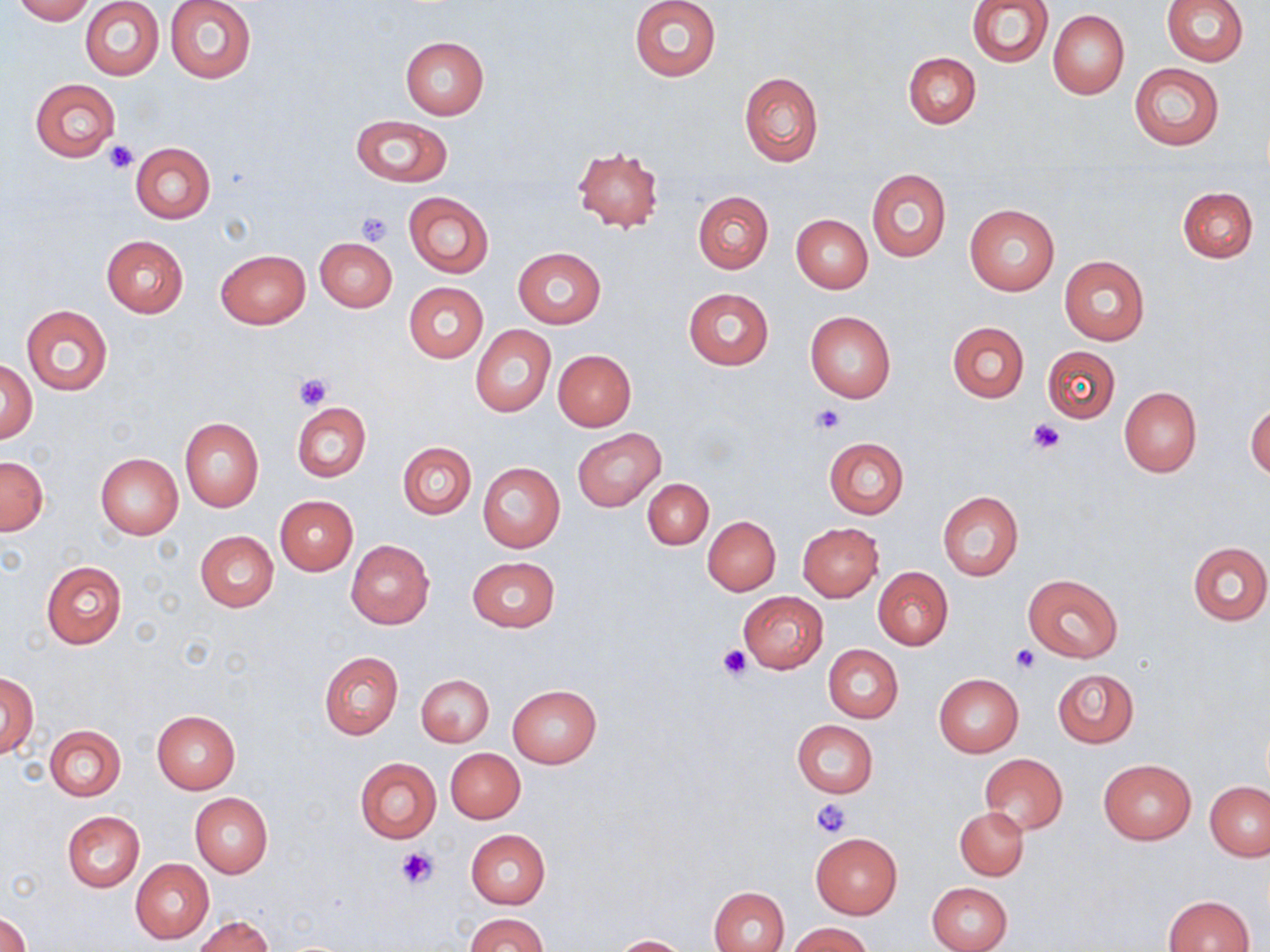
Summary:
  - Coordinate format: approximate bounding boxes as (x1, y1, x2, y2) in pixels
  - Platelet locations: (106, 139, 138, 173), (356, 210, 395, 245), (293, 373, 332, 410), (809, 405, 843, 433), (1027, 420, 1064, 454), (718, 645, 751, 680), (1012, 645, 1040, 672), (811, 798, 852, 839), (396, 845, 440, 889)
  - Uninfected red blood cell locations: (13, 0, 93, 23), (165, 0, 256, 83), (629, 0, 721, 82), (967, 0, 1053, 67), (1161, 0, 1248, 65), (81, 2, 164, 80), (1049, 9, 1129, 99), (401, 36, 489, 118), (904, 53, 980, 129), (1129, 63, 1224, 151), (739, 72, 823, 167), (31, 79, 119, 161), (350, 114, 454, 187), (129, 143, 215, 224), (572, 147, 664, 232), (866, 169, 951, 262), (1177, 187, 1258, 262), (404, 191, 493, 278), (693, 191, 773, 274), (964, 204, 1060, 295), (792, 214, 872, 293), (101, 236, 188, 317), (316, 237, 397, 312), (512, 248, 604, 329), (215, 249, 310, 328), (1059, 256, 1150, 345), (404, 283, 487, 362), (684, 287, 773, 370), (22, 305, 112, 395), (804, 311, 896, 402), (947, 320, 1029, 403), (470, 325, 555, 417), (1043, 345, 1119, 422), (553, 350, 636, 430), (1, 358, 36, 444), (1119, 387, 1201, 478), (1247, 401, 1270, 481), (292, 402, 371, 481), (179, 417, 264, 511), (572, 428, 666, 512), (825, 437, 909, 519), (398, 442, 476, 518), (96, 454, 183, 539), (1, 456, 48, 535), (477, 463, 565, 552), (642, 478, 714, 549), (937, 491, 1023, 580), (274, 495, 358, 575), (703, 515, 780, 596), (797, 522, 884, 601), (195, 531, 279, 611), (346, 540, 435, 629), (1187, 540, 1270, 625), (466, 556, 559, 632), (41, 561, 126, 648), (873, 567, 953, 649), (1024, 575, 1124, 661), (738, 591, 828, 672), (824, 645, 903, 723), (319, 652, 403, 739), (1053, 669, 1138, 747), (0, 671, 37, 759), (417, 673, 494, 747), (934, 674, 1024, 758), (507, 685, 602, 768), (151, 710, 240, 793), (791, 719, 878, 797), (45, 725, 125, 800), (446, 748, 524, 823), (979, 754, 1068, 833), (354, 757, 441, 844), (1098, 758, 1197, 845), (1205, 781, 1270, 861), (190, 792, 273, 877), (954, 806, 1028, 881), (61, 811, 144, 893), (466, 829, 550, 908), (810, 833, 902, 918), (130, 859, 215, 944), (928, 882, 1013, 952), (711, 887, 789, 952), (1164, 895, 1254, 952), (0, 912, 32, 952), (467, 913, 548, 952), (194, 915, 274, 952), (786, 922, 871, 952), (612, 935, 689, 951)
  - Slide-level diagnosis: no evidence of blood parasites
  - Stain: May-Grünwald-Giemsa
  - Modality: optical microscopy
  - Field of view: one of a larger specimen
  - Magnification: 1000x
  - Preparation: thin blood smear
  - Image size: 1270×952 pixels